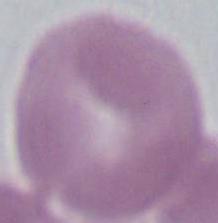 Captured at 1000x magnification. An erythrocyte is seen. Photomicrograph.